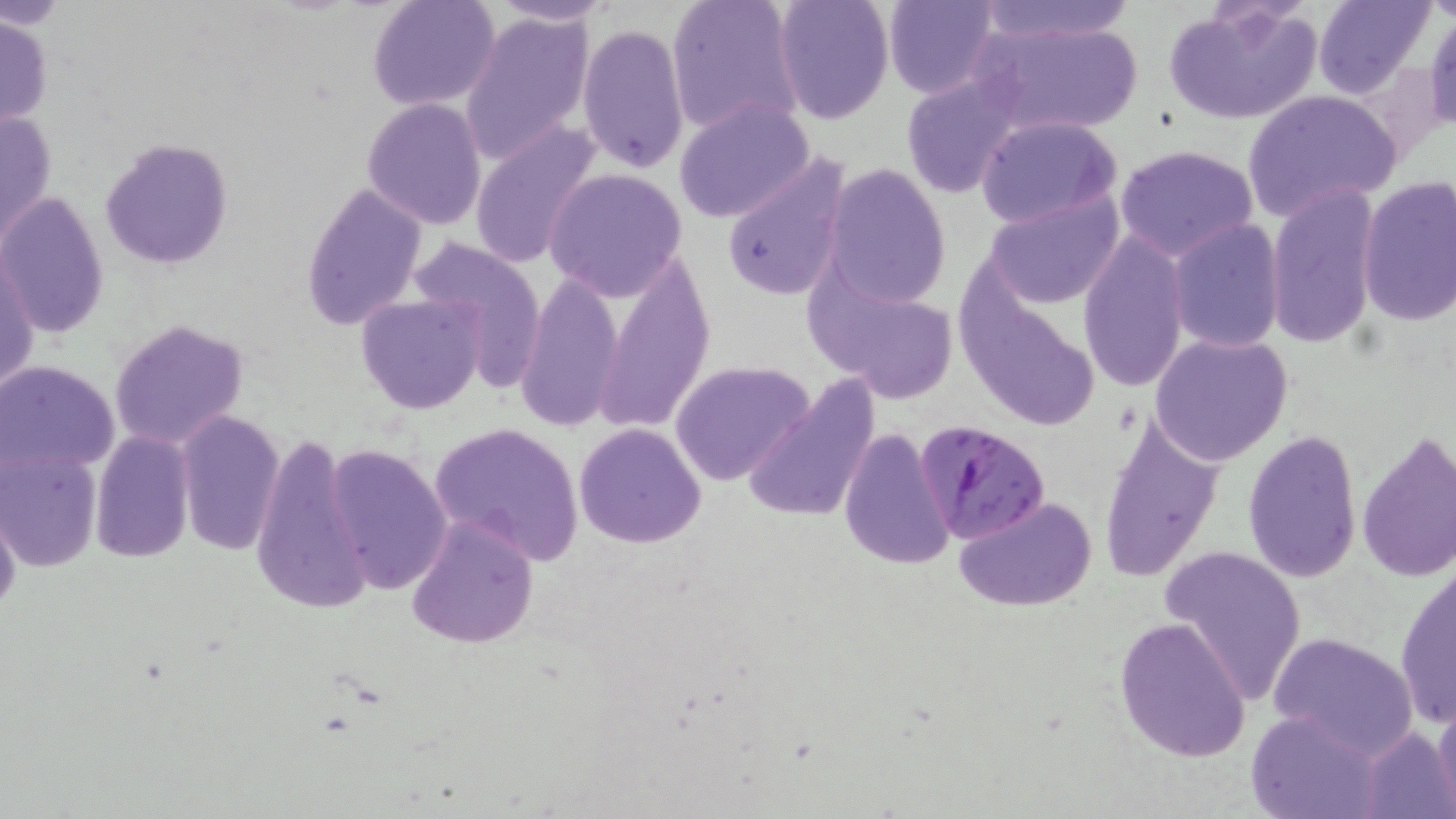
slide-level diagnosis = Plasmodium falciparum
uninfected red blood cell locations = approximate bounding boxes as named x1/y1/x2/y2 corners in pixels: (x1=367, y1=0, x2=500, y2=112), (x1=489, y1=0, x2=620, y2=26), (x1=665, y1=0, x2=805, y2=138), (x1=771, y1=0, x2=894, y2=123), (x1=883, y1=0, x2=998, y2=99), (x1=972, y1=0, x2=1141, y2=45), (x1=1315, y1=0, x2=1432, y2=98), (x1=1160, y1=4, x2=1323, y2=124), (x1=460, y1=10, x2=596, y2=163), (x1=1425, y1=11, x2=1456, y2=134), (x1=1, y1=14, x2=53, y2=132), (x1=971, y1=17, x2=1145, y2=136), (x1=577, y1=23, x2=690, y2=173), (x1=899, y1=74, x2=1024, y2=198), (x1=1243, y1=89, x2=1402, y2=220), (x1=674, y1=98, x2=816, y2=225), (x1=362, y1=99, x2=486, y2=228), (x1=1, y1=106, x2=58, y2=251), (x1=975, y1=115, x2=1122, y2=229), (x1=468, y1=123, x2=604, y2=269), (x1=100, y1=136, x2=235, y2=270), (x1=1115, y1=144, x2=1259, y2=261), (x1=722, y1=154, x2=852, y2=303), (x1=822, y1=163, x2=951, y2=307), (x1=545, y1=168, x2=688, y2=301), (x1=1356, y1=175, x2=1456, y2=325), (x1=301, y1=182, x2=426, y2=329), (x1=1266, y1=183, x2=1380, y2=350), (x1=982, y1=191, x2=1126, y2=309), (x1=0, y1=192, x2=107, y2=340), (x1=1168, y1=219, x2=1285, y2=353), (x1=1077, y1=229, x2=1191, y2=394), (x1=413, y1=241, x2=547, y2=388), (x1=1, y1=247, x2=40, y2=399), (x1=594, y1=259, x2=715, y2=436), (x1=806, y1=267, x2=965, y2=404), (x1=518, y1=273, x2=622, y2=431), (x1=354, y1=295, x2=486, y2=416), (x1=108, y1=318, x2=250, y2=451), (x1=1150, y1=333, x2=1293, y2=466), (x1=671, y1=359, x2=814, y2=485), (x1=0, y1=360, x2=121, y2=475), (x1=740, y1=374, x2=882, y2=526), (x1=1096, y1=410, x2=1225, y2=584), (x1=175, y1=412, x2=284, y2=557), (x1=428, y1=421, x2=586, y2=565), (x1=574, y1=422, x2=706, y2=548), (x1=839, y1=426, x2=956, y2=570), (x1=1242, y1=428, x2=1362, y2=584), (x1=89, y1=431, x2=194, y2=564), (x1=251, y1=433, x2=369, y2=617), (x1=1355, y1=433, x2=1456, y2=585), (x1=324, y1=443, x2=452, y2=597), (x1=0, y1=449, x2=102, y2=572), (x1=954, y1=495, x2=1100, y2=611), (x1=0, y1=506, x2=21, y2=627), (x1=405, y1=514, x2=538, y2=650), (x1=1159, y1=546, x2=1308, y2=703), (x1=1395, y1=563, x2=1455, y2=729), (x1=1115, y1=616, x2=1252, y2=762), (x1=1267, y1=630, x2=1419, y2=756), (x1=1433, y1=698, x2=1455, y2=817), (x1=1246, y1=710, x2=1384, y2=819), (x1=1356, y1=726, x2=1454, y2=819)
magnification = 1000x
stain = May-Grünwald-Giemsa
preparation = thin blood smear
image size = 1456×819 pixels
modality = optical microscopy
Plasmodium falciparum-infected red blood cell locations = approximate bounding boxes as named x1/y1/x2/y2 corners in pixels: (x1=912, y1=418, x2=1052, y2=547)
field of view = one of a larger specimen